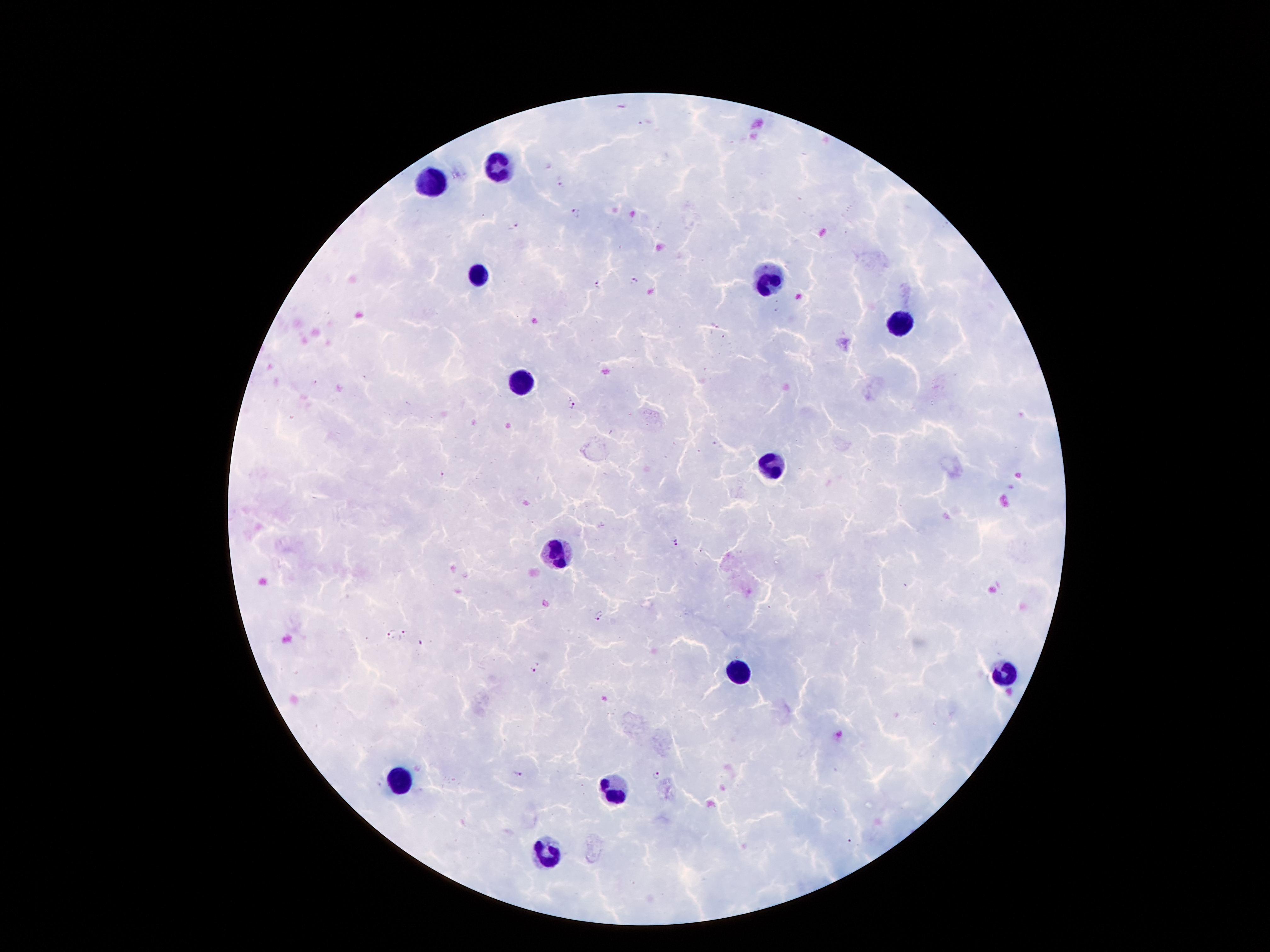

coordinate format = approximate centers as [x, y] in pixels
malaria parasite locations = [560, 179], [576, 213], [512, 224], [634, 282], [596, 285], [571, 404], [442, 475], [675, 539], [598, 614], [405, 633], [391, 634], [536, 668], [516, 774], [657, 774]
leukocyte locations = [496, 167], [426, 183], [478, 274], [766, 283], [900, 326], [521, 383], [771, 465], [559, 551], [737, 672], [1002, 674], [400, 781], [611, 788], [546, 851]
capture = smartphone camera through the microscope eyepiece
image size = 1270×952 pixels
magnification = 100x
field of view = single
stain = Giemsa
patient malaria status = positive for Plasmodium falciparum
preparation = thick blood smear